Assess this cell for malaria.
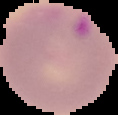
Parasitized.

From a thin blood smear. Cell region segmented out of the field of view; the surrounding area is masked to black. Image is 118×115 pixels.